Assess this cell for malaria.
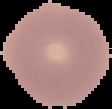
Uninfected.

{
  "image_size": "112×109 pixels",
  "image_type": "segmented cell region on a black background",
  "preparation": "thin blood smear"
}